Point out leukocytes.
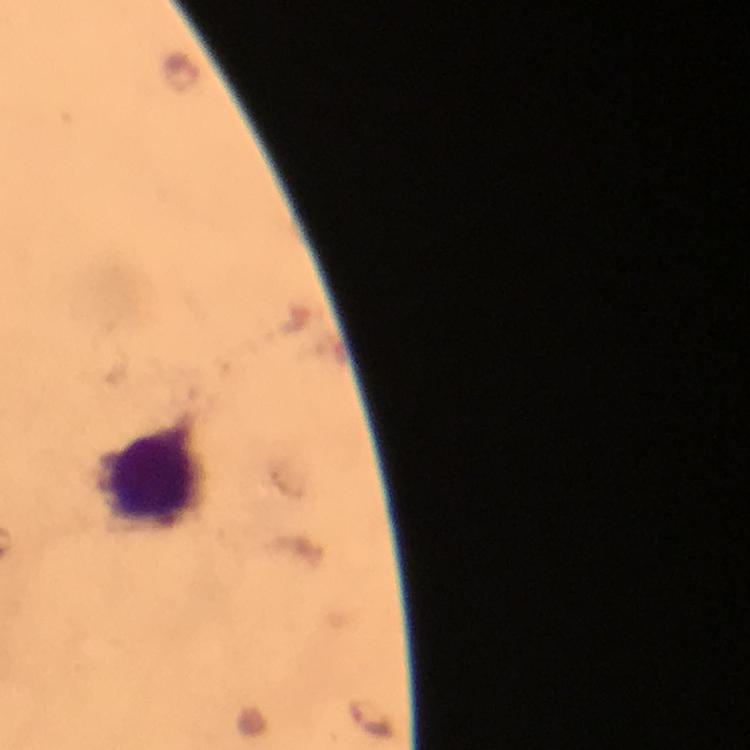

Approximate centers as (x, y) in pixels.
Leukocytes: (155, 477).

context = from a diagnostic examination for malaria
cropped from = one field of view
Plasmodium parasite locations = approximate centers as (x, y) in pixels: (372, 719)
immersion oil = applied
image size = 750×750 pixels
preparation = thick blood film
stain = Giemsa
capture = smartphone photograph through a microscope
magnification = 100x